Classify this cell by malaria status.
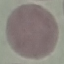

Uninfected.

Summary:
  - Capture: smartphone through the microscope eyepiece
  - Preparation: thin smear
  - Stain: Giemsa
  - Image type: automatically extracted cell patch, resized to 64 × 64 pixels